Report the malaria status of this cell.
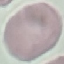

Uninfected.

Summary:
  - Image type: automatically extracted cell patch, resized to 64 × 64 pixels
  - Preparation: thin smear
  - Stain: Giemsa
  - Capture: smartphone through the microscope eyepiece